Name the blood parasite species.
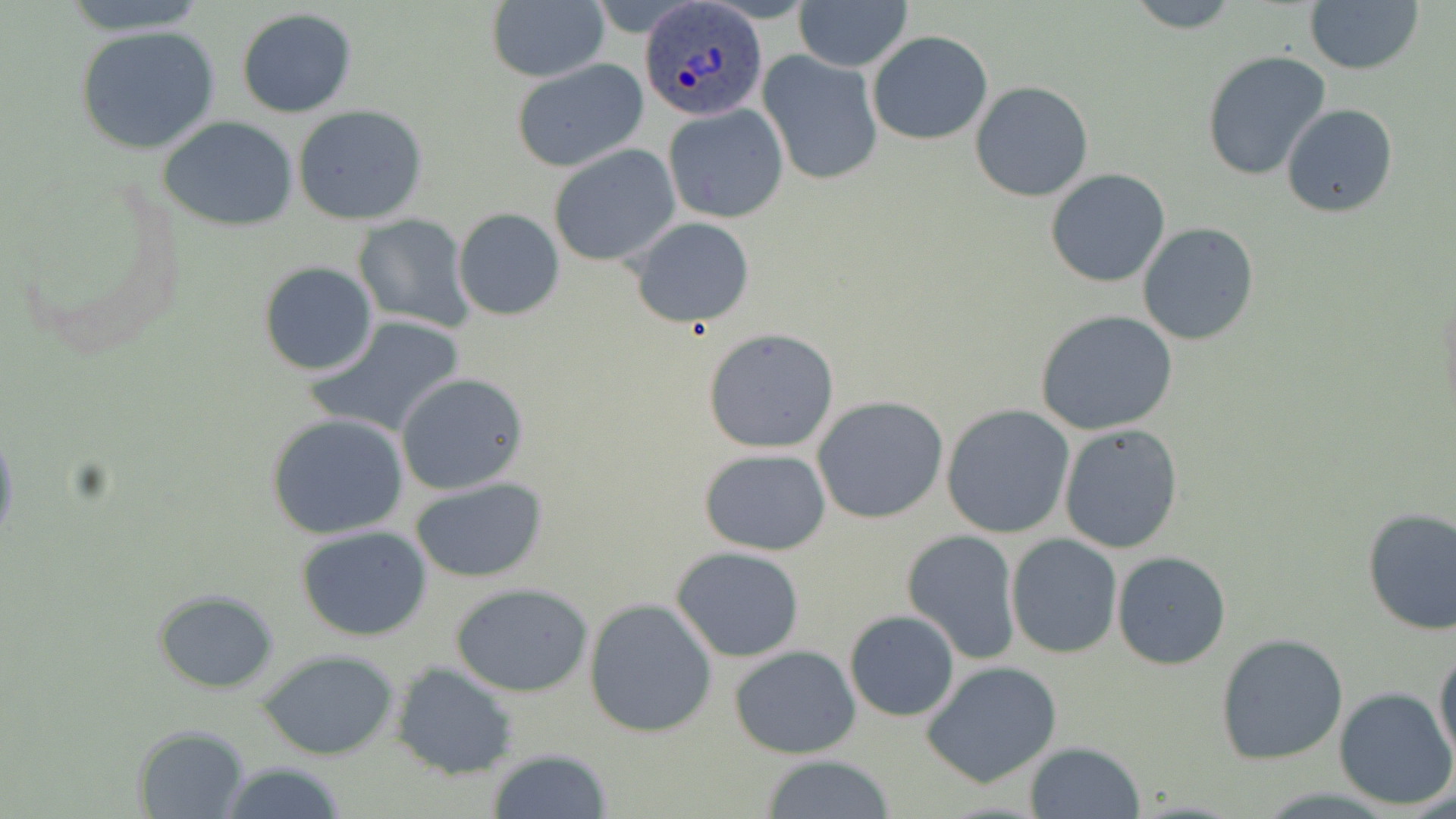
Plasmodium ovale.

Summary:
  - Coordinate format: approximate bounding boxes as named x1/y1/x2/y2 corners in pixels
  - Plasmodium ovale-infected red blood cell locations: (x1=641, y1=2, x2=765, y2=122)
  - Uninfected red blood cell locations: (x1=60, y1=0, x2=209, y2=35), (x1=486, y1=0, x2=609, y2=83), (x1=793, y1=0, x2=911, y2=70), (x1=1121, y1=0, x2=1243, y2=33), (x1=1304, y1=0, x2=1425, y2=74), (x1=235, y1=9, x2=358, y2=116), (x1=73, y1=24, x2=226, y2=157), (x1=867, y1=30, x2=993, y2=144), (x1=758, y1=49, x2=884, y2=188), (x1=1201, y1=49, x2=1332, y2=182), (x1=509, y1=58, x2=648, y2=172), (x1=970, y1=82, x2=1095, y2=201), (x1=663, y1=102, x2=789, y2=224), (x1=1281, y1=103, x2=1398, y2=217), (x1=292, y1=104, x2=430, y2=227), (x1=156, y1=115, x2=301, y2=233), (x1=547, y1=144, x2=681, y2=267), (x1=1046, y1=168, x2=1170, y2=288), (x1=453, y1=208, x2=564, y2=321), (x1=352, y1=214, x2=474, y2=331), (x1=627, y1=216, x2=755, y2=327), (x1=1136, y1=222, x2=1258, y2=346), (x1=258, y1=261, x2=379, y2=377), (x1=1034, y1=309, x2=1178, y2=435), (x1=304, y1=316, x2=468, y2=439), (x1=703, y1=327, x2=840, y2=454), (x1=394, y1=372, x2=529, y2=496), (x1=812, y1=397, x2=950, y2=522), (x1=941, y1=404, x2=1075, y2=539), (x1=265, y1=412, x2=411, y2=539), (x1=1058, y1=424, x2=1183, y2=554), (x1=0, y1=428, x2=20, y2=550), (x1=698, y1=448, x2=830, y2=556), (x1=406, y1=476, x2=551, y2=584), (x1=1361, y1=507, x2=1456, y2=636), (x1=295, y1=527, x2=435, y2=643), (x1=902, y1=528, x2=1022, y2=664), (x1=1006, y1=534, x2=1122, y2=659), (x1=670, y1=546, x2=806, y2=662), (x1=1112, y1=551, x2=1231, y2=670), (x1=451, y1=582, x2=595, y2=697), (x1=152, y1=588, x2=281, y2=694), (x1=582, y1=597, x2=718, y2=738), (x1=844, y1=610, x2=961, y2=721), (x1=1215, y1=632, x2=1350, y2=764), (x1=728, y1=645, x2=861, y2=759), (x1=1433, y1=647, x2=1456, y2=766), (x1=256, y1=649, x2=404, y2=761), (x1=922, y1=661, x2=1064, y2=786), (x1=391, y1=662, x2=518, y2=780), (x1=1334, y1=687, x2=1454, y2=810), (x1=132, y1=724, x2=253, y2=817), (x1=1024, y1=742, x2=1144, y2=818), (x1=484, y1=748, x2=614, y2=819), (x1=759, y1=755, x2=899, y2=817), (x1=214, y1=761, x2=351, y2=819)
  - Image size: 1456×819 pixels
  - Magnification: 1000x
  - Field of view: single
  - Stain: May-Grünwald-Giemsa
  - Modality: optical microscopy
  - Preparation: thin blood smear